Assess this cell for malaria.
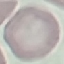
Uninfected.

Acquired by smartphone through the microscope eyepiece. Cell patch, automatically extracted from a larger field of view and resized to 64 × 64 pixels. Giemsa-stained preparation. Thin blood film.